State which parasite is depicted.
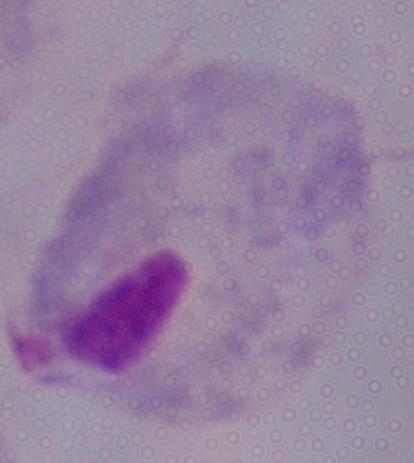

A trichomonad.

Summary:
  - Modality: photomicrograph
  - Magnification: 1000x